Report the malaria status of this cell.
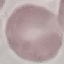

Uninfected.

{
  "capture": "smartphone through the microscope eyepiece",
  "image_type": "automatically extracted cell patch, resized to 64 × 64 pixels",
  "preparation": "thin blood film",
  "stain": "Giemsa"
}